Locate and identify every blood parasite.
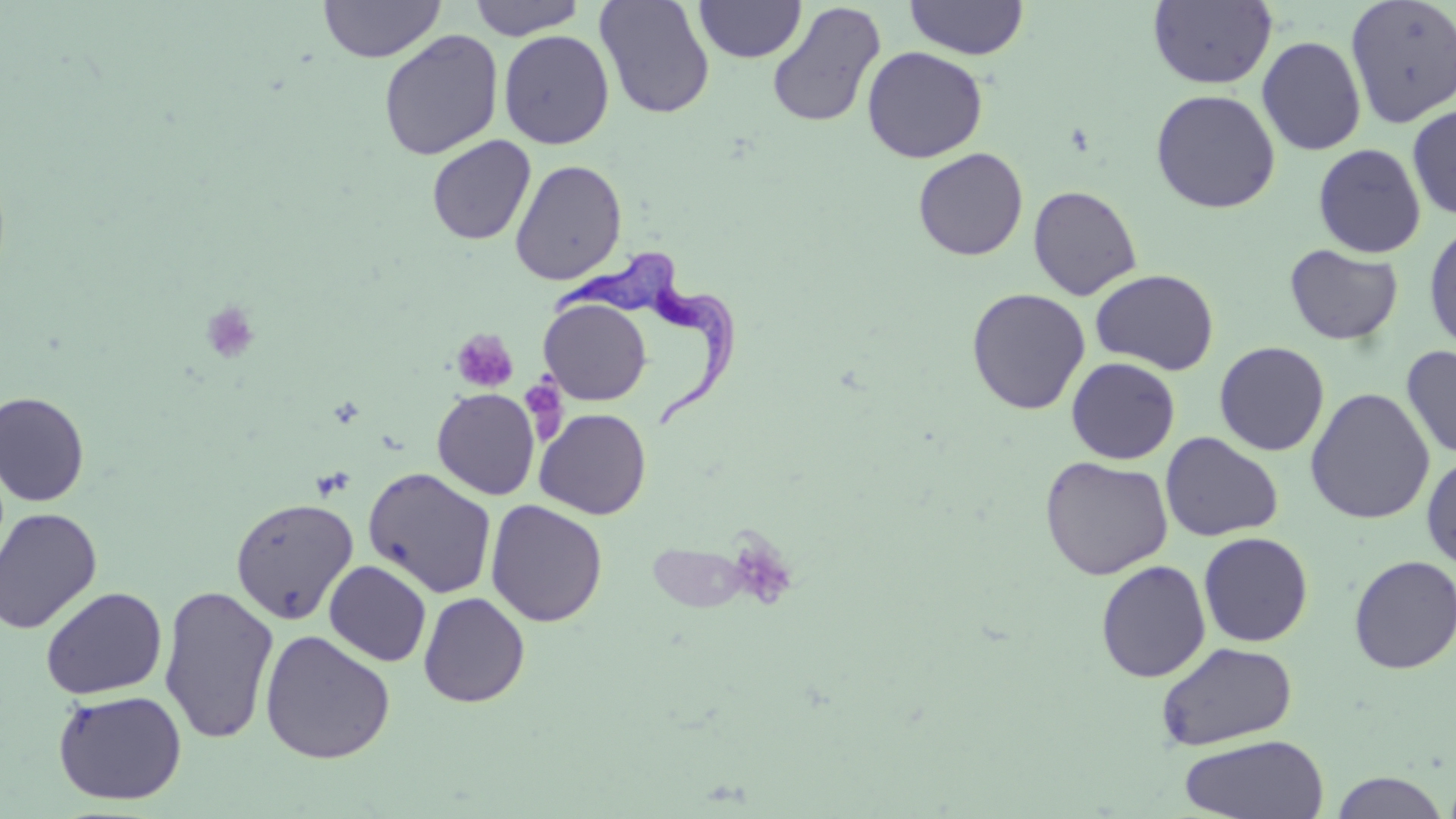
Approximate bounding boxes as named x1/y1/x2/y2 corners in pixels.
Trypanosoma brucei: (x1=550, y1=250, x2=741, y2=434).
No Plasmodium falciparum, Plasmodium ovale, Plasmodium malariae, Plasmodium vivax, or Babesia divergens observed.

Summary:
  - Platelet locations: (x1=200, y1=301, x2=261, y2=364), (x1=451, y1=328, x2=518, y2=394), (x1=524, y1=370, x2=571, y2=444), (x1=735, y1=532, x2=795, y2=609)
  - Uninfected red blood cell locations: (x1=319, y1=0, x2=444, y2=62), (x1=469, y1=0, x2=585, y2=39), (x1=595, y1=0, x2=715, y2=119), (x1=695, y1=0, x2=806, y2=62), (x1=905, y1=0, x2=1029, y2=60), (x1=1147, y1=0, x2=1278, y2=89), (x1=1345, y1=0, x2=1456, y2=129), (x1=766, y1=2, x2=886, y2=128), (x1=498, y1=29, x2=614, y2=149), (x1=378, y1=30, x2=504, y2=161), (x1=1257, y1=36, x2=1367, y2=155), (x1=861, y1=46, x2=988, y2=163), (x1=1149, y1=89, x2=1281, y2=213), (x1=1407, y1=104, x2=1456, y2=219), (x1=427, y1=135, x2=536, y2=246), (x1=1313, y1=143, x2=1427, y2=258), (x1=913, y1=147, x2=1028, y2=261), (x1=510, y1=159, x2=627, y2=285), (x1=1028, y1=185, x2=1142, y2=301), (x1=1423, y1=221, x2=1456, y2=355), (x1=1284, y1=244, x2=1403, y2=345), (x1=1090, y1=269, x2=1219, y2=375), (x1=966, y1=288, x2=1091, y2=415), (x1=539, y1=298, x2=652, y2=406), (x1=1213, y1=341, x2=1330, y2=456), (x1=1401, y1=345, x2=1456, y2=460), (x1=1066, y1=357, x2=1180, y2=465), (x1=432, y1=388, x2=540, y2=500), (x1=1304, y1=388, x2=1435, y2=525), (x1=0, y1=390, x2=90, y2=506), (x1=534, y1=408, x2=651, y2=520), (x1=1160, y1=432, x2=1283, y2=542), (x1=1420, y1=453, x2=1456, y2=570), (x1=1039, y1=456, x2=1173, y2=580), (x1=363, y1=467, x2=497, y2=598), (x1=230, y1=497, x2=358, y2=624), (x1=485, y1=499, x2=608, y2=627), (x1=0, y1=507, x2=103, y2=634), (x1=1198, y1=531, x2=1313, y2=647), (x1=1348, y1=554, x2=1456, y2=675), (x1=324, y1=560, x2=432, y2=666), (x1=1095, y1=560, x2=1211, y2=683), (x1=159, y1=582, x2=279, y2=746), (x1=39, y1=586, x2=168, y2=699), (x1=418, y1=591, x2=530, y2=707), (x1=259, y1=629, x2=396, y2=764), (x1=1155, y1=641, x2=1298, y2=750), (x1=52, y1=689, x2=187, y2=806), (x1=1178, y1=734, x2=1330, y2=819), (x1=1330, y1=771, x2=1451, y2=818)
  - Slide-level diagnosis: Trypanosoma brucei
  - Preparation: thin blood smear
  - Image size: 1456×819 pixels
  - Magnification: 1000x
  - Field of view: one of a larger specimen
  - Stain: May-Grünwald-Giemsa
  - Modality: light microscopy